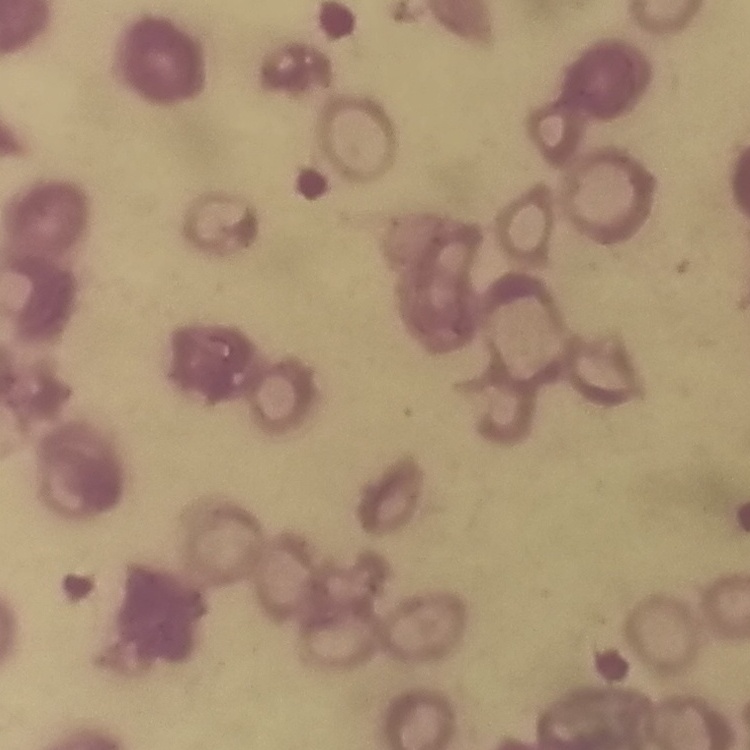
Summary:
  - Red blood cell morphology: rouleaux formation
  - Image type: one tile cut from a larger photomicrograph
  - Stain: Field's or Giemsa
  - Preparation: thin blood film